Outline each uninfected red blood cell.
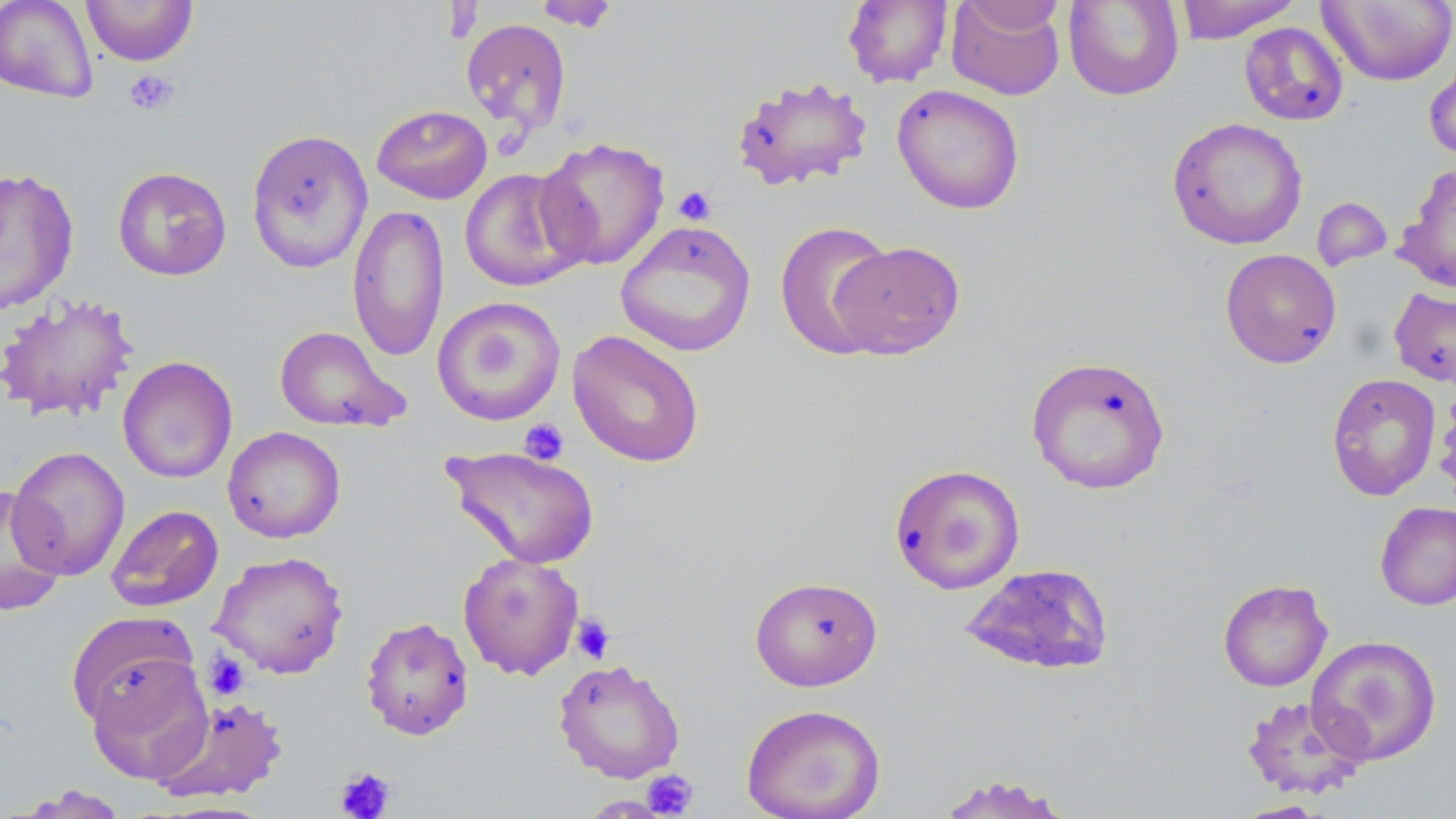
Approximate bounding boxes as (x1, y1, x2, y2) in pixels.
Uninfected red blood cells: (0, 0, 99, 104), (80, 0, 199, 66), (533, 0, 620, 31), (842, 0, 953, 88), (946, 0, 1065, 100), (1063, 0, 1184, 101), (1174, 0, 1302, 43), (1318, 0, 1456, 87), (961, 1, 1067, 37), (461, 18, 571, 135), (1239, 22, 1349, 126), (1424, 53, 1456, 166), (731, 76, 874, 192), (892, 84, 1025, 215), (371, 104, 493, 204), (1166, 117, 1308, 250), (245, 128, 373, 274), (535, 136, 671, 271), (1396, 163, 1455, 294), (112, 166, 232, 281), (458, 167, 590, 292), (0, 168, 80, 313), (1311, 197, 1393, 272), (347, 203, 450, 363), (775, 219, 897, 359), (615, 220, 757, 357), (829, 240, 966, 360), (1220, 248, 1342, 369), (1388, 286, 1456, 388), (0, 293, 139, 423), (432, 296, 566, 426), (274, 325, 406, 432), (566, 329, 705, 468), (1025, 353, 1171, 494), (117, 356, 238, 484), (1327, 373, 1441, 501), (1435, 385, 1456, 506), (222, 426, 346, 543), (6, 445, 131, 581), (442, 445, 602, 569), (889, 463, 1025, 595), (0, 486, 65, 615), (1375, 501, 1456, 611), (106, 504, 224, 612), (210, 551, 349, 679), (458, 552, 584, 680), (958, 562, 1115, 676), (750, 575, 883, 691), (1217, 579, 1333, 692), (66, 611, 200, 730), (360, 616, 475, 741), (1306, 635, 1441, 766), (84, 652, 213, 783), (553, 658, 686, 783), (154, 695, 288, 804), (1241, 695, 1370, 799), (741, 703, 886, 819), (933, 774, 1076, 818), (14, 785, 130, 818), (1232, 800, 1331, 818).

slide_level_diagnosis: no evidence of blood parasites
image_size: 1456×819 pixels
magnification: 1000x
stain: May-Grünwald-Giemsa
platelet_locations: 'approximate bounding boxes as (x1, y1, x2, y2) in pixels: (123, 68, 179, 115), (673, 185, 717, 226), (519, 418, 569, 465), (571, 613, 615, 664), (204, 651, 249, 700), (335, 766, 396, 819), (641, 769, 699, 817)'
field_of_view: single
modality: light microscopy
preparation: thin blood smear